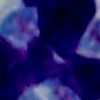

{
  "identification": "leukocyte",
  "modality": "micrograph",
  "magnification": "1000x"
}